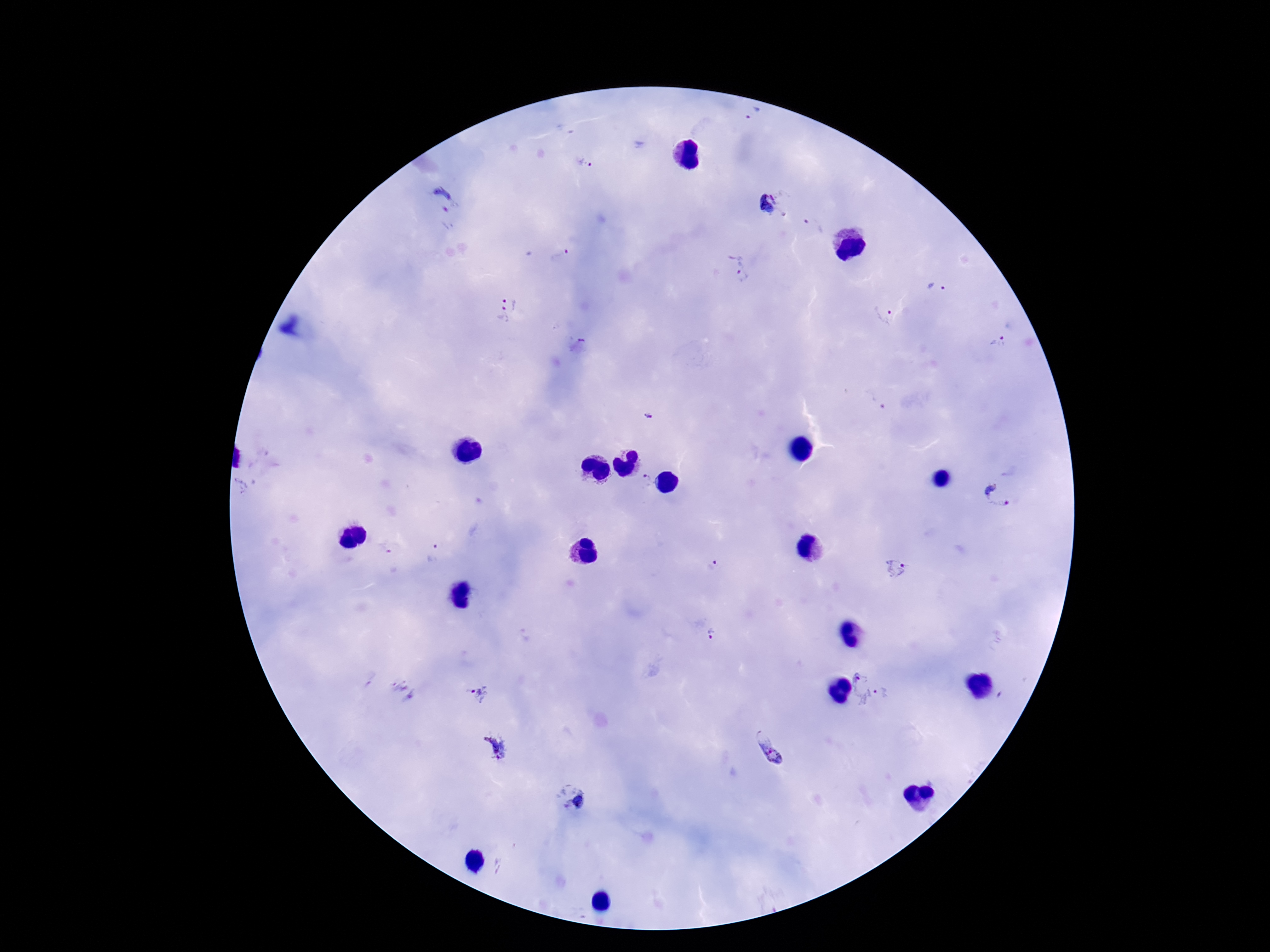
Approximate centers as {x, y} in pixels.
Summary:
  - Plasmodium parasite locations: {753, 114}, {566, 128}, {584, 162}, {442, 200}, {769, 204}, {814, 224}, {561, 256}, {740, 269}, {935, 287}, {506, 309}, {882, 314}, {581, 340}, {999, 343}, {875, 401}, {648, 416}, {646, 482}, {999, 493}, {386, 547}, {436, 555}, {713, 565}, {899, 570}, {713, 634}, {860, 689}, {886, 692}, {402, 693}, {479, 693}, {497, 748}, {773, 749}, {573, 797}
  - Magnification: 100x
  - Capture: smartphone camera through the microscope eyepiece
  - Patient malaria status: positive
  - Field of view: single
  - Image size: 1270×952 pixels
  - Preparation: thick blood smear
  - Stain: Giemsa